Locate every Plasmodium parasite.
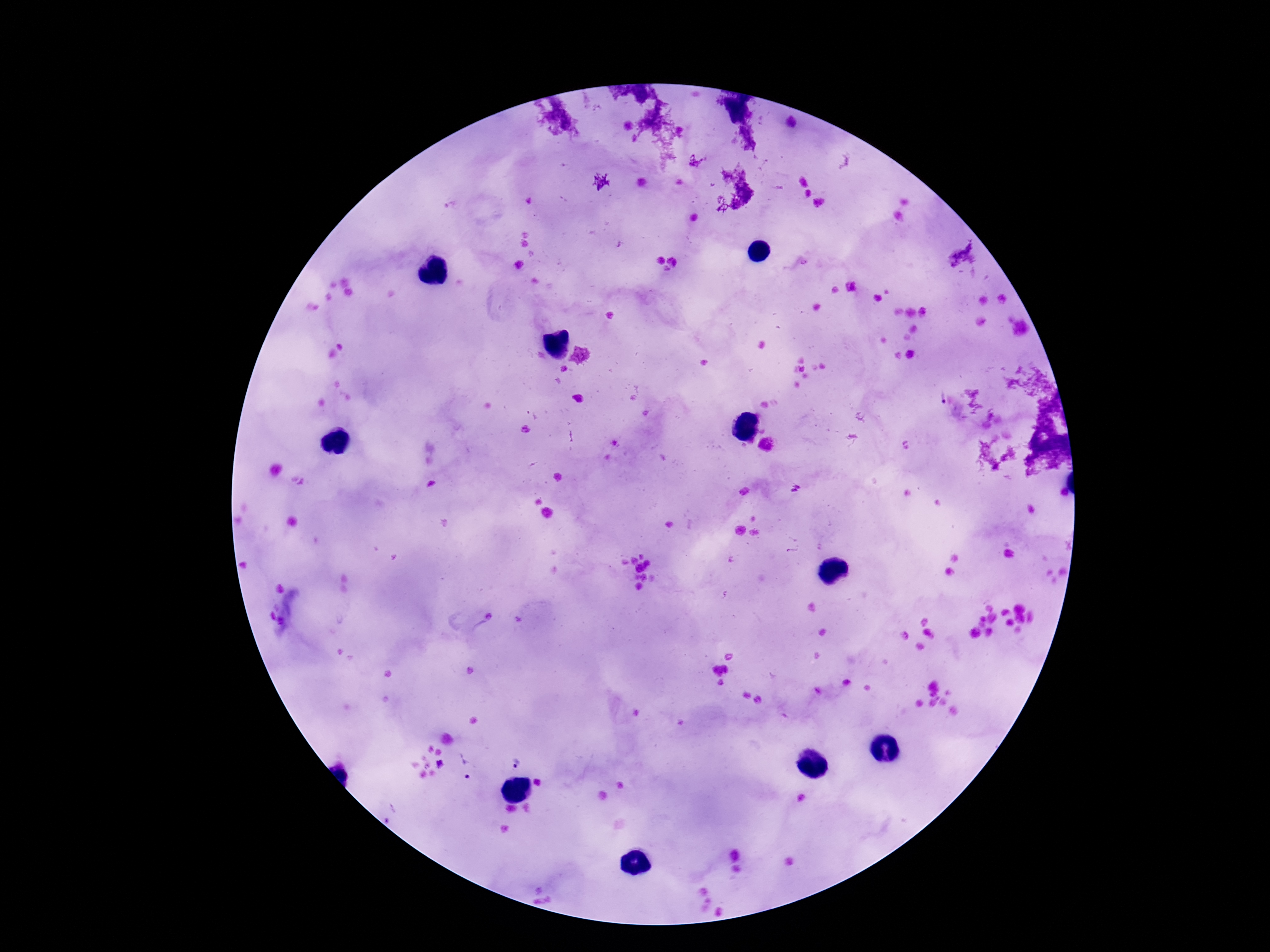

Approximate centers as [x, y] in pixels.
Plasmodium parasites: [938, 398], [515, 762], [439, 764], [469, 766].

Summary:
  - Field of view: single
  - Image size: 1270×952 pixels
  - Patient malaria status: infected
  - Capture: smartphone camera through the microscope eyepiece
  - Preparation: thick blood smear
  - Magnification: 100x
  - Stain: Giemsa